Comment on the morphology of the erythrocytes.
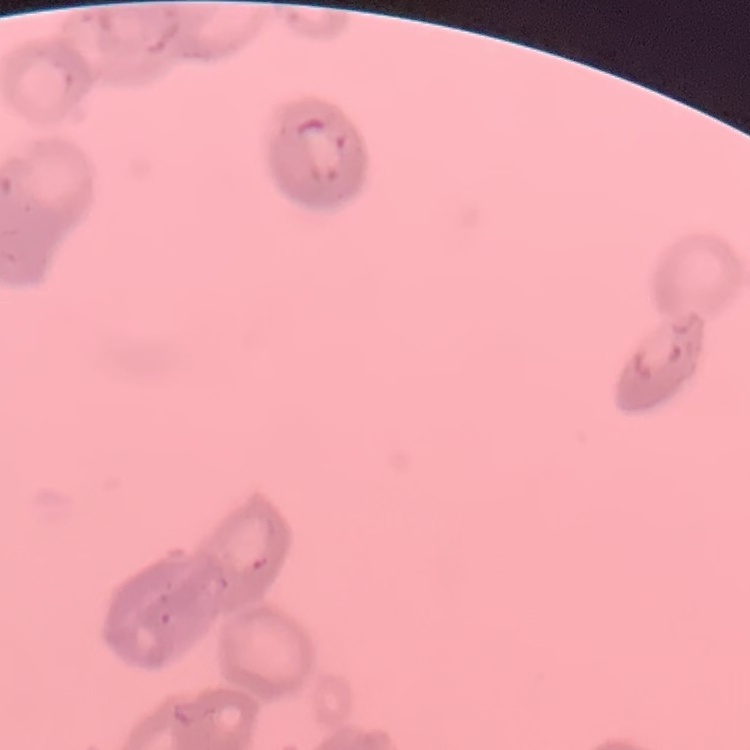
Rouleaux formation.

Summary:
  - Image type: one tile cut from a larger photomicrograph
  - Preparation: thin peripheral smear
  - Stain: Field's or Giemsa